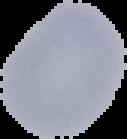

image_type: segmented cell region with the area outside set to black
preparation: thin blood smear
image_size: 127×139 pixels
malaria_status: uninfected